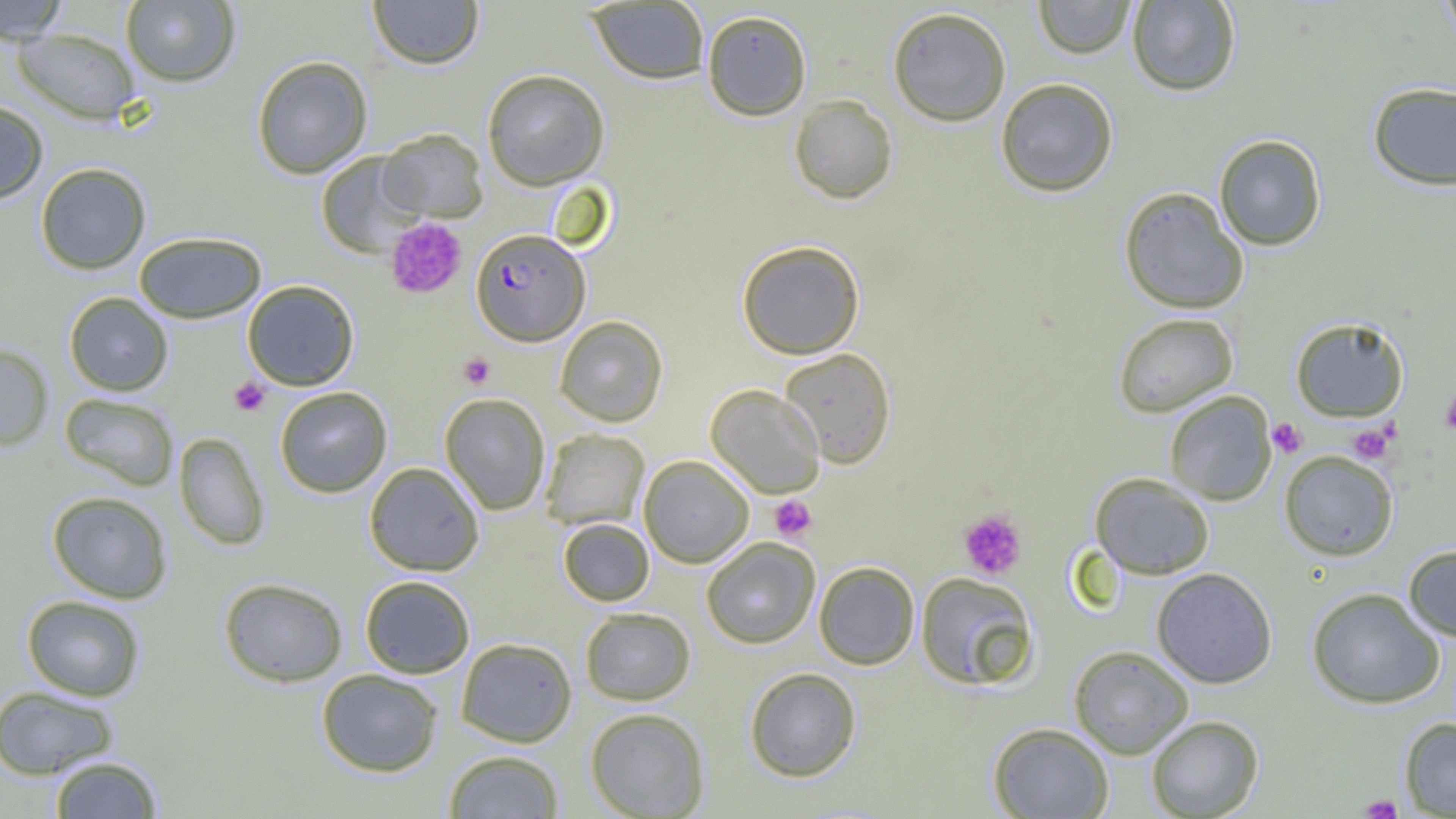
slide-level diagnosis = Plasmodium falciparum
modality = light microscopy
uninfected red blood cell locations = approximate bounding boxes as (x1, y1, x2, y2) in pixels: (0, 0, 70, 45), (121, 0, 241, 87), (368, 0, 483, 70), (1033, 0, 1136, 58), (1437, 0, 1456, 47), (587, 1, 710, 85), (1127, 1, 1241, 96), (886, 6, 1012, 127), (701, 9, 812, 121), (12, 27, 141, 124), (252, 55, 373, 179), (482, 69, 610, 191), (995, 78, 1119, 197), (1367, 82, 1456, 191), (789, 94, 898, 204), (0, 100, 49, 203), (377, 128, 488, 222), (1214, 134, 1327, 251), (315, 151, 424, 257), (35, 162, 151, 274), (1118, 186, 1249, 315), (134, 231, 266, 323), (736, 240, 864, 359), (242, 280, 359, 391), (64, 292, 173, 396), (1113, 312, 1239, 418), (554, 315, 668, 427), (1290, 317, 1408, 421), (0, 343, 54, 451), (778, 347, 897, 469), (705, 384, 825, 497), (274, 386, 392, 497), (1164, 391, 1277, 505), (59, 392, 180, 491), (439, 392, 551, 515), (540, 428, 649, 529), (173, 432, 270, 550), (1279, 450, 1399, 561), (639, 455, 754, 567), (364, 461, 485, 576), (1089, 472, 1215, 580), (46, 490, 173, 603), (558, 518, 654, 606), (700, 537, 821, 649), (1403, 545, 1456, 641), (814, 561, 920, 670), (1151, 567, 1278, 688), (915, 571, 1041, 691), (359, 575, 475, 679), (218, 577, 348, 687), (1306, 587, 1446, 709), (21, 595, 145, 701), (579, 607, 696, 706), (456, 637, 577, 747), (1069, 645, 1194, 759), (744, 667, 861, 782), (316, 669, 444, 777), (0, 685, 120, 780), (585, 707, 711, 818), (1146, 715, 1264, 818), (1399, 717, 1456, 817), (988, 722, 1114, 819), (443, 749, 565, 818), (48, 755, 164, 818)
field of view = one of a larger specimen
magnification = 1000x
Plasmodium falciparum-infected red blood cell locations = approximate bounding boxes as (x1, y1, x2, y2) in pixels: (471, 228, 589, 345)
platelet locations = approximate bounding boxes as (x1, y1, x2, y2) in pixels: (384, 218, 467, 300), (459, 353, 496, 389), (229, 377, 270, 416), (1441, 387, 1456, 434), (1268, 417, 1307, 458), (1348, 422, 1394, 463), (769, 495, 817, 541), (958, 508, 1028, 580), (1359, 794, 1403, 818)
preparation = thin blood film
image size = 1456×819 pixels